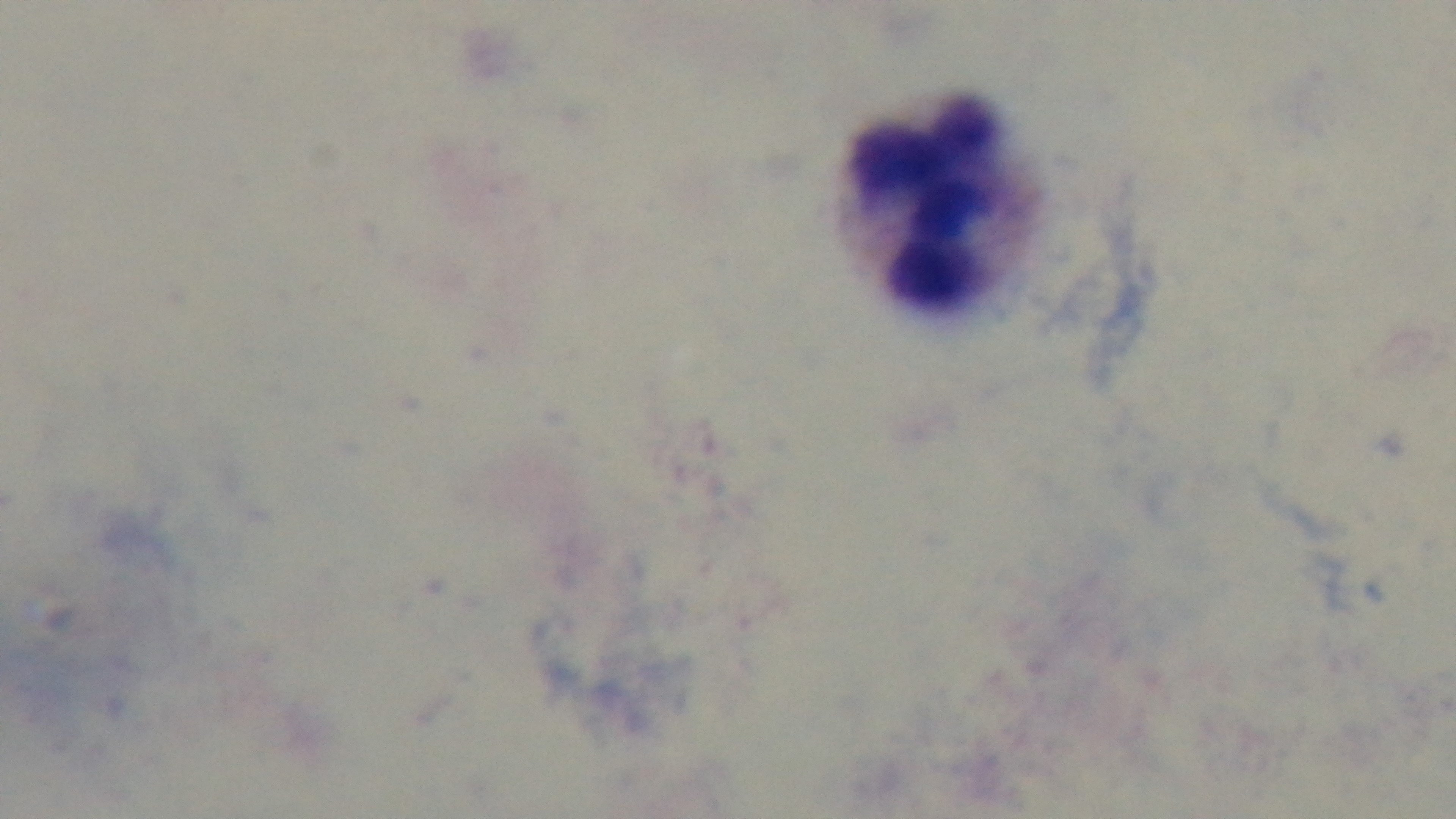
modality = light microscopy
objective = 100x oil immersion
preparation = thick
malaria status = uninfected
field of view = single
stain = Giemsa
capture = mounted 4K digital camera